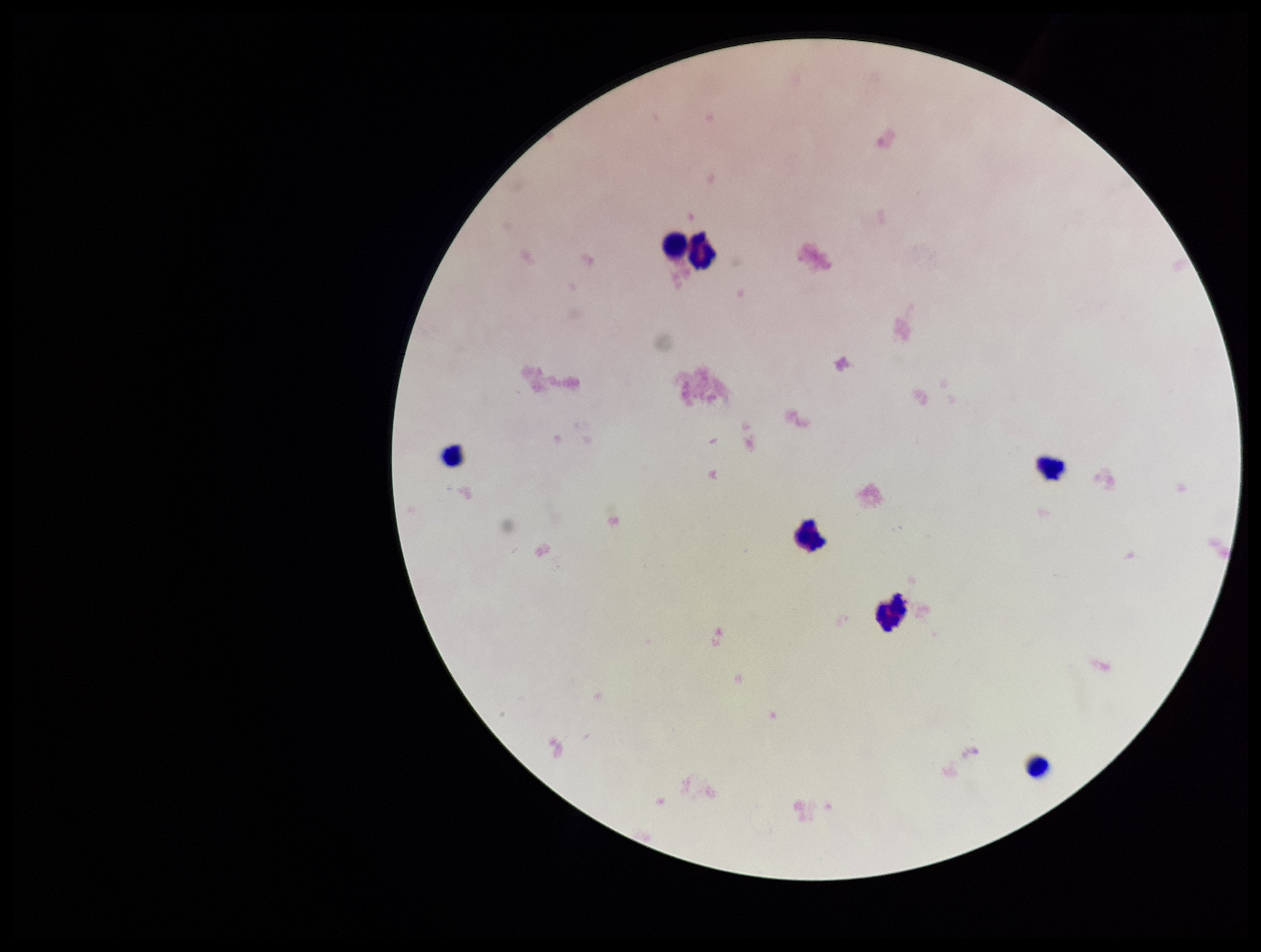

Summary:
  - Stain: Giemsa
  - Preparation: thick blood smear
  - Image size: 1261×952 pixels
  - Parasite count: 0
  - Capture: smartphone photograph through the microscope eyepiece
  - Leukocyte count: 7
  - Field of view: single
  - Plasmodium parasites: none seen
  - Patient malaria status: negative